Assess the morphology of the erythrocytes.
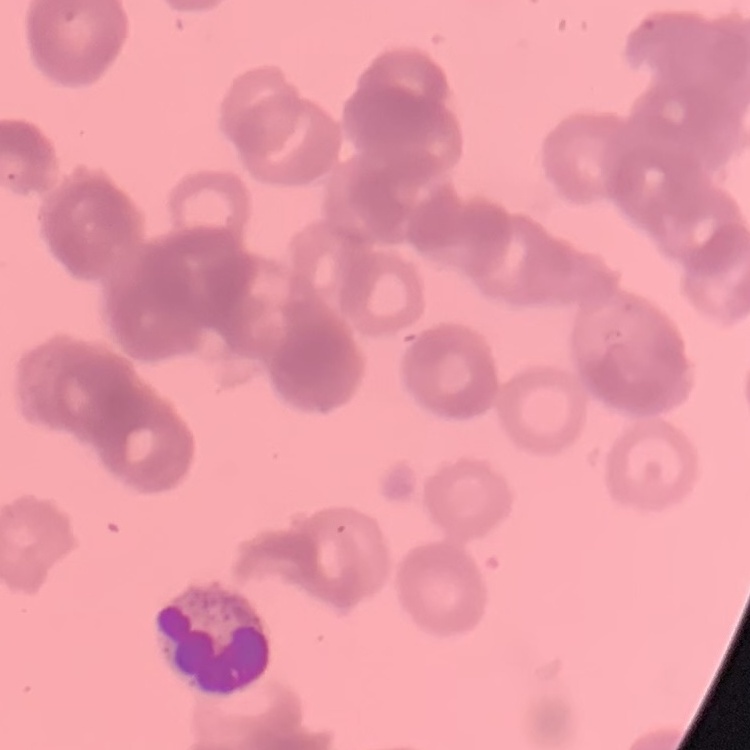
Rouleaux formation.

Summary:
  - Stain: Field's or Giemsa
  - Image type: square crop of a larger photomicrograph
  - Preparation: thin blood smear